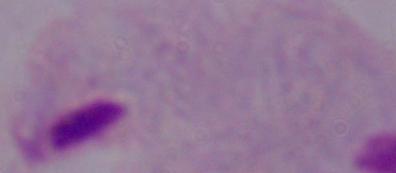

Summary:
  - Identification: trichomonad
  - Magnification: 1000x
  - Modality: micrograph